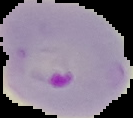

Malaria status: parasitized. From a thin blood smear. Cell region segmented out of the field of view; the surrounding area is masked to black. Image is 133×118 pixels.